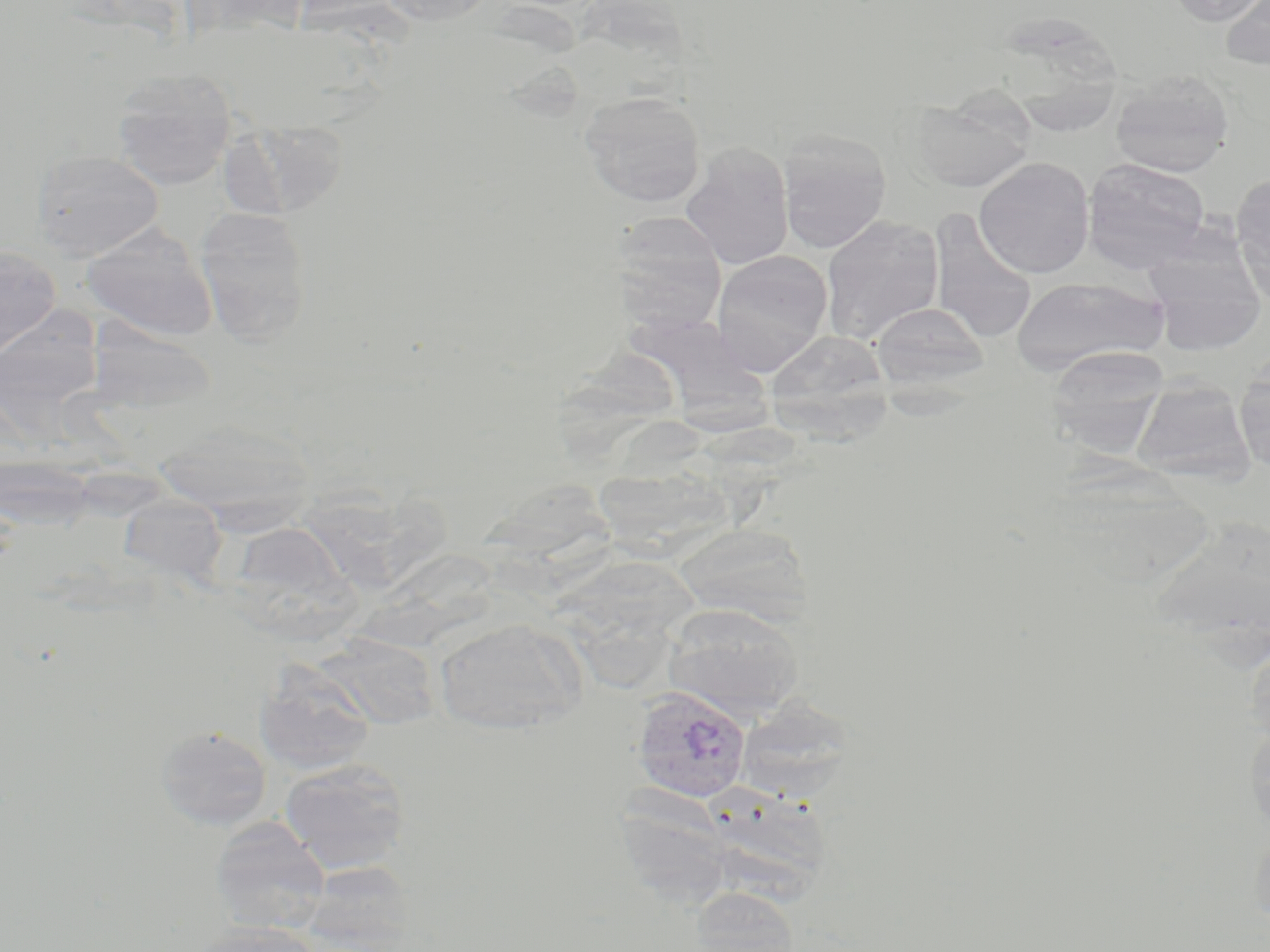

Summary:
  - Coordinate format: approximate bounding boxes as [x1, y1, x2, y2] in pixels
  - Uninfected red blood cell locations: [379, 0, 495, 26], [1165, 0, 1269, 26], [1220, 0, 1270, 72], [1004, 11, 1125, 137], [111, 68, 237, 189], [1110, 72, 1234, 177], [911, 89, 1036, 192], [579, 91, 707, 207], [228, 127, 349, 218], [777, 129, 892, 253], [680, 142, 794, 270], [32, 149, 163, 260], [974, 157, 1095, 278], [1082, 158, 1212, 272], [1231, 174, 1270, 296], [195, 206, 313, 345], [929, 211, 1039, 345], [609, 212, 731, 326], [820, 215, 944, 344], [80, 223, 218, 342], [0, 246, 61, 356], [711, 249, 832, 374], [1145, 249, 1267, 355], [1010, 276, 1166, 373], [870, 301, 989, 390], [2, 302, 105, 419], [633, 307, 779, 448], [82, 313, 225, 425], [764, 329, 894, 438], [1047, 346, 1168, 458], [555, 347, 687, 465], [1235, 357, 1270, 471], [1132, 378, 1256, 484], [152, 421, 315, 523], [598, 451, 744, 570], [305, 464, 452, 590], [486, 487, 626, 608], [118, 493, 228, 586], [224, 521, 359, 638], [673, 522, 811, 625], [358, 539, 512, 654], [566, 559, 695, 699], [662, 603, 804, 720], [433, 617, 587, 734], [1244, 633, 1270, 748], [316, 634, 443, 729], [253, 660, 377, 776], [734, 698, 855, 804], [1245, 721, 1270, 840], [154, 725, 272, 830], [279, 759, 411, 874], [713, 783, 839, 909], [623, 788, 739, 914], [210, 818, 330, 935], [701, 894, 807, 952], [187, 921, 321, 952]
  - Plasmodium vivax-infected red blood cell locations: [630, 685, 752, 803]
  - Slide-level diagnosis: Plasmodium vivax
  - Modality: optical microscopy
  - Stain: May-Grünwald-Giemsa
  - Preparation: thin blood smear
  - Image size: 1270×952 pixels
  - Magnification: 1000x
  - Field of view: single